Classify this cell by malaria status.
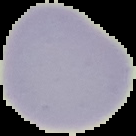

It is uninfected.

Cell region segmented out of the field of view; the surrounding area is masked to black. From a thin blood smear. Image is 136×136 pixels.